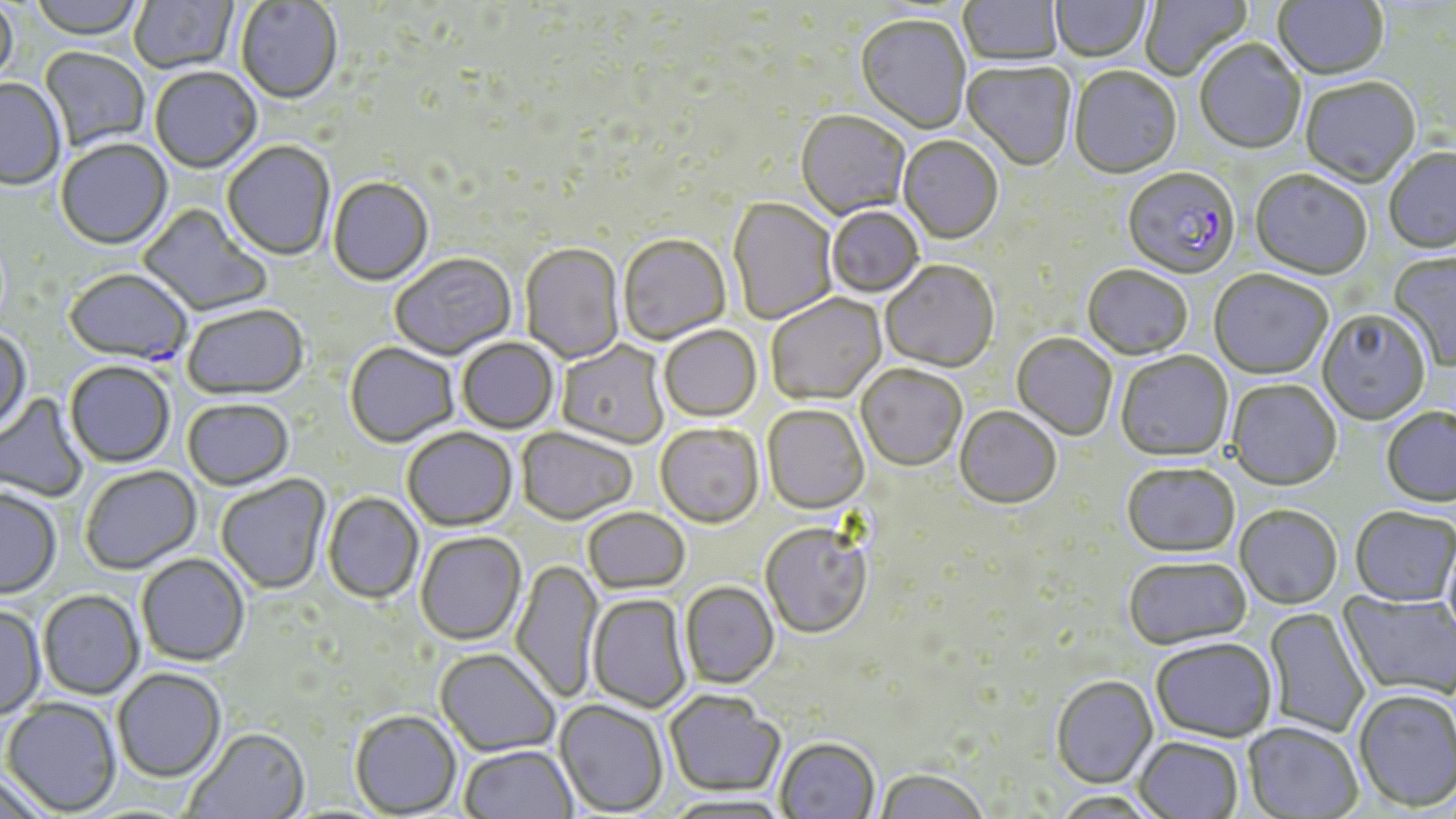 Approximate bounding boxes as (x1, y1, x2, y2) in pixels. Plasmodium falciparum-infected red blood cell locations: (1122, 170, 1239, 281), (63, 270, 193, 367). Uninfected red blood cell locations: (28, 0, 147, 41), (129, 0, 239, 75), (959, 0, 1063, 68), (1051, 0, 1150, 65), (1140, 0, 1251, 81), (1273, 0, 1388, 82), (235, 1, 343, 106), (0, 2, 18, 90), (855, 16, 970, 136), (1194, 41, 1306, 156), (38, 48, 150, 152), (962, 62, 1076, 173), (1069, 68, 1183, 181), (150, 69, 262, 175), (1300, 79, 1421, 189), (0, 80, 66, 191), (796, 112, 910, 220), (898, 137, 1003, 246), (56, 140, 173, 252), (223, 143, 335, 262), (1384, 150, 1456, 256), (1250, 171, 1371, 282), (328, 178, 434, 288), (728, 199, 837, 325), (137, 204, 272, 318), (826, 207, 924, 299), (618, 236, 731, 347), (520, 244, 625, 365), (1387, 253, 1456, 371), (390, 254, 516, 361), (881, 262, 999, 374), (1082, 267, 1192, 361), (1209, 272, 1332, 381), (766, 294, 887, 407), (182, 306, 309, 402), (1317, 311, 1430, 426), (658, 326, 762, 423), (0, 329, 32, 436), (1011, 334, 1117, 441), (456, 338, 558, 434), (556, 341, 670, 450), (345, 344, 459, 449), (1116, 352, 1233, 462), (64, 362, 175, 469), (856, 366, 966, 472), (1226, 381, 1342, 492), (0, 393, 89, 503), (182, 400, 294, 492), (762, 406, 870, 515), (955, 408, 1061, 510), (1380, 408, 1456, 508), (655, 425, 764, 530), (517, 428, 637, 526), (402, 429, 518, 532), (1122, 465, 1239, 559), (80, 466, 202, 574), (216, 475, 331, 596), (0, 490, 61, 600), (323, 492, 424, 604), (1234, 507, 1342, 611), (583, 508, 690, 596), (1350, 509, 1456, 609), (760, 523, 872, 639), (415, 532, 526, 646), (1441, 536, 1456, 648), (136, 555, 250, 667), (1123, 558, 1252, 651), (511, 560, 603, 702), (680, 582, 780, 690), (38, 591, 144, 700), (1338, 591, 1456, 700), (587, 594, 692, 713), (0, 606, 46, 721), (1262, 607, 1369, 737), (1151, 640, 1276, 744), (435, 650, 560, 758), (113, 669, 226, 783), (1051, 676, 1158, 790), (664, 690, 785, 797), (1353, 690, 1456, 814), (2, 698, 121, 816), (555, 700, 668, 816), (350, 711, 462, 817), (1242, 724, 1363, 818), (185, 728, 310, 819), (775, 738, 879, 819), (1134, 738, 1243, 819), (459, 745, 577, 819), (874, 769, 988, 819), (0, 772, 55, 819), (662, 793, 792, 818), (1048, 793, 1161, 818). Slide-level diagnosis: Plasmodium falciparum. One field of a larger specimen. Image is 1456×819 pixels. Thin blood film. May-Grünwald-Giemsa stain. Light microscopy. 1000x magnification.